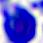
magnification: 400x
modality: photomicrograph
identification: white blood cell